Describe the morphology of the erythrocytes.
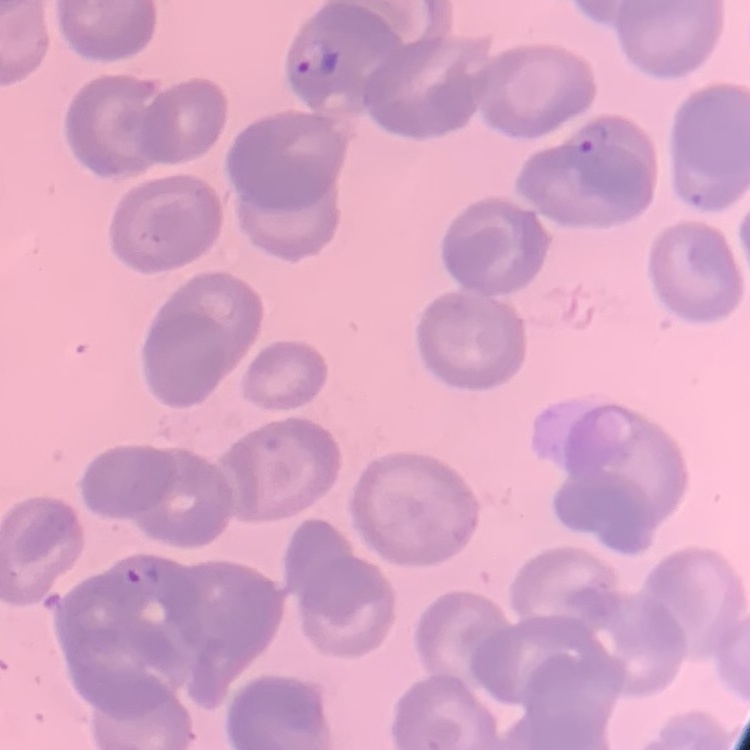
They show no rouleaux formation.

Summary:
  - Image type: one tile cut from a larger photomicrograph
  - Stain: Field's or Giemsa
  - Preparation: thin blood film